Classify this cell by malaria status.
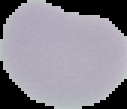

Uninfected.

Summary:
  - Image size: 127×109 pixels
  - Image type: segmented cell region on a black background
  - Preparation: thin blood smear